Locate and identify every blood parasite.
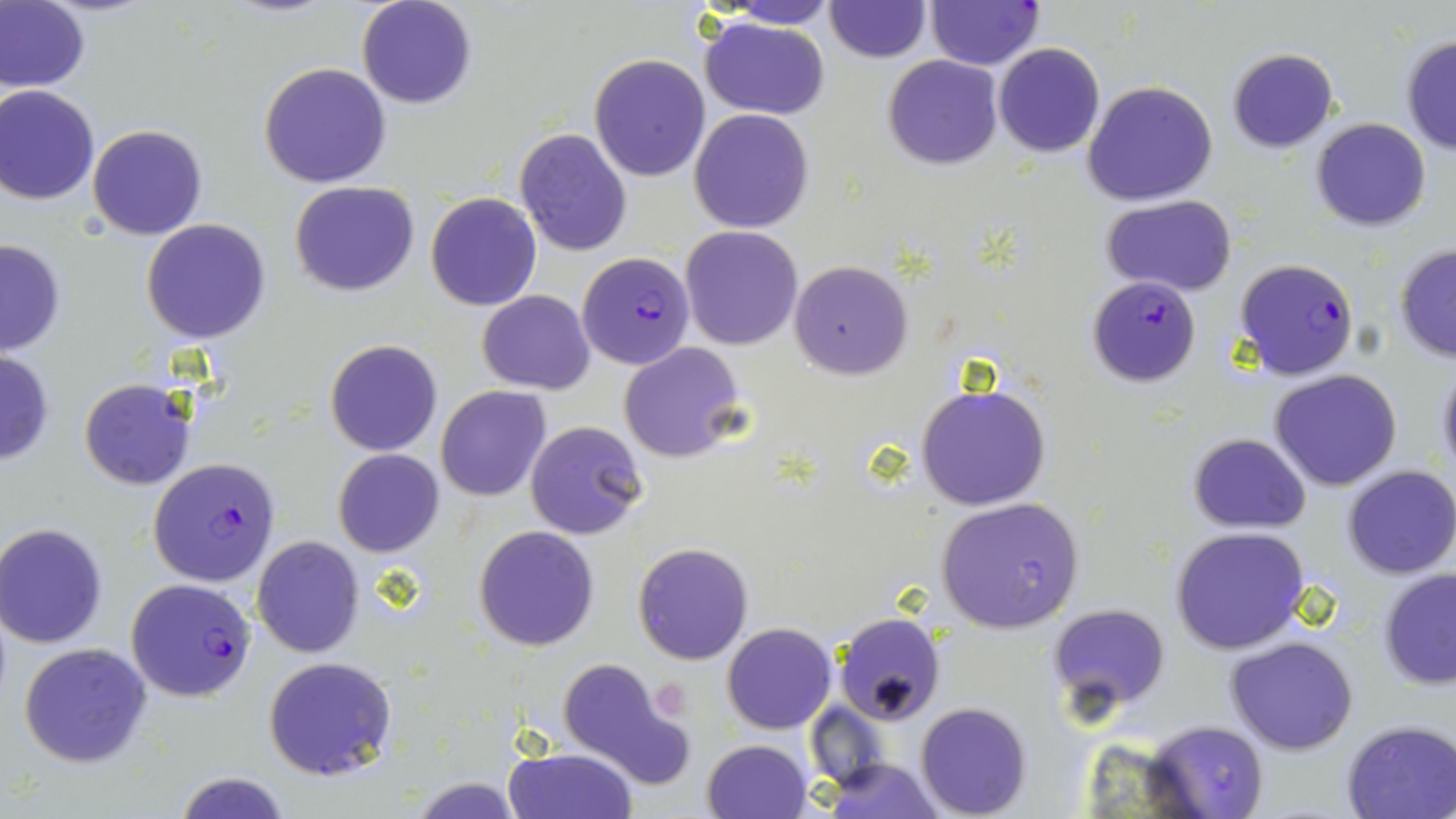

Approximate bounding boxes as named x1/y1/x2/y2 corners in pixels.
Plasmodium falciparum-infected red blood cells: (x1=926, y1=1, x2=1043, y2=69), (x1=576, y1=251, x2=695, y2=369), (x1=1234, y1=258, x2=1359, y2=381), (x1=1087, y1=276, x2=1200, y2=387), (x1=148, y1=459, x2=281, y2=586), (x1=125, y1=577, x2=257, y2=702).
No Plasmodium ovale, Plasmodium malariae, Plasmodium vivax, Babesia divergens, or Trypanosoma brucei observed.

Summary:
  - Platelet locations: (x1=657, y1=684, x2=690, y2=723)
  - Uninfected red blood cell locations: (x1=358, y1=0, x2=477, y2=109), (x1=0, y1=1, x2=89, y2=93), (x1=715, y1=1, x2=839, y2=28), (x1=825, y1=1, x2=930, y2=63), (x1=700, y1=16, x2=831, y2=119), (x1=1400, y1=35, x2=1456, y2=154), (x1=993, y1=43, x2=1106, y2=158), (x1=1226, y1=47, x2=1338, y2=152), (x1=590, y1=53, x2=710, y2=181), (x1=883, y1=55, x2=1002, y2=170), (x1=259, y1=62, x2=392, y2=189), (x1=1083, y1=80, x2=1219, y2=207), (x1=0, y1=85, x2=101, y2=206), (x1=689, y1=109, x2=815, y2=233), (x1=1311, y1=117, x2=1431, y2=232), (x1=87, y1=125, x2=207, y2=240), (x1=514, y1=128, x2=632, y2=256), (x1=289, y1=180, x2=420, y2=296), (x1=426, y1=192, x2=541, y2=311), (x1=1101, y1=193, x2=1239, y2=296), (x1=140, y1=220, x2=271, y2=343), (x1=680, y1=226, x2=802, y2=350), (x1=0, y1=237, x2=68, y2=355), (x1=1394, y1=244, x2=1456, y2=362), (x1=789, y1=259, x2=913, y2=379), (x1=477, y1=290, x2=596, y2=394), (x1=325, y1=339, x2=444, y2=457), (x1=618, y1=342, x2=745, y2=462), (x1=0, y1=347, x2=55, y2=468), (x1=1434, y1=359, x2=1456, y2=485), (x1=1269, y1=369, x2=1403, y2=492), (x1=79, y1=379, x2=195, y2=490), (x1=915, y1=381, x2=1051, y2=512), (x1=435, y1=386, x2=550, y2=501), (x1=524, y1=419, x2=649, y2=540), (x1=1187, y1=433, x2=1311, y2=532), (x1=333, y1=449, x2=444, y2=558), (x1=1344, y1=464, x2=1456, y2=579), (x1=936, y1=497, x2=1083, y2=632), (x1=1, y1=524, x2=112, y2=649), (x1=1170, y1=525, x2=1311, y2=655), (x1=474, y1=526, x2=600, y2=651), (x1=252, y1=535, x2=364, y2=657), (x1=632, y1=542, x2=754, y2=665), (x1=1378, y1=569, x2=1456, y2=691), (x1=1047, y1=603, x2=1172, y2=723), (x1=833, y1=611, x2=947, y2=724), (x1=721, y1=623, x2=837, y2=734), (x1=1227, y1=637, x2=1359, y2=754), (x1=18, y1=641, x2=153, y2=768), (x1=263, y1=656, x2=397, y2=781), (x1=557, y1=657, x2=690, y2=790), (x1=916, y1=702, x2=1032, y2=818), (x1=806, y1=703, x2=893, y2=789), (x1=1338, y1=718, x2=1456, y2=819), (x1=1142, y1=720, x2=1269, y2=817), (x1=703, y1=738, x2=813, y2=818), (x1=505, y1=745, x2=636, y2=819), (x1=816, y1=757, x2=946, y2=817), (x1=174, y1=772, x2=293, y2=818), (x1=408, y1=776, x2=524, y2=817)
  - Slide-level diagnosis: Plasmodium falciparum
  - Field of view: one of a larger specimen
  - Image size: 1456×819 pixels
  - Preparation: thin blood smear
  - Magnification: 1000x
  - Modality: optical microscopy
  - Stain: May-Grünwald-Giemsa